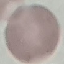

malaria status = uninfected
capture = smartphone camera at the microscope eyepiece
stain = Giemsa
preparation = thin blood smear
image type = automatically extracted cell patch, resized to 64 × 64 pixels